Locate the cells, classifying each as a parasitized red blood cell, an uninfected red blood cell, or a white blood cell.
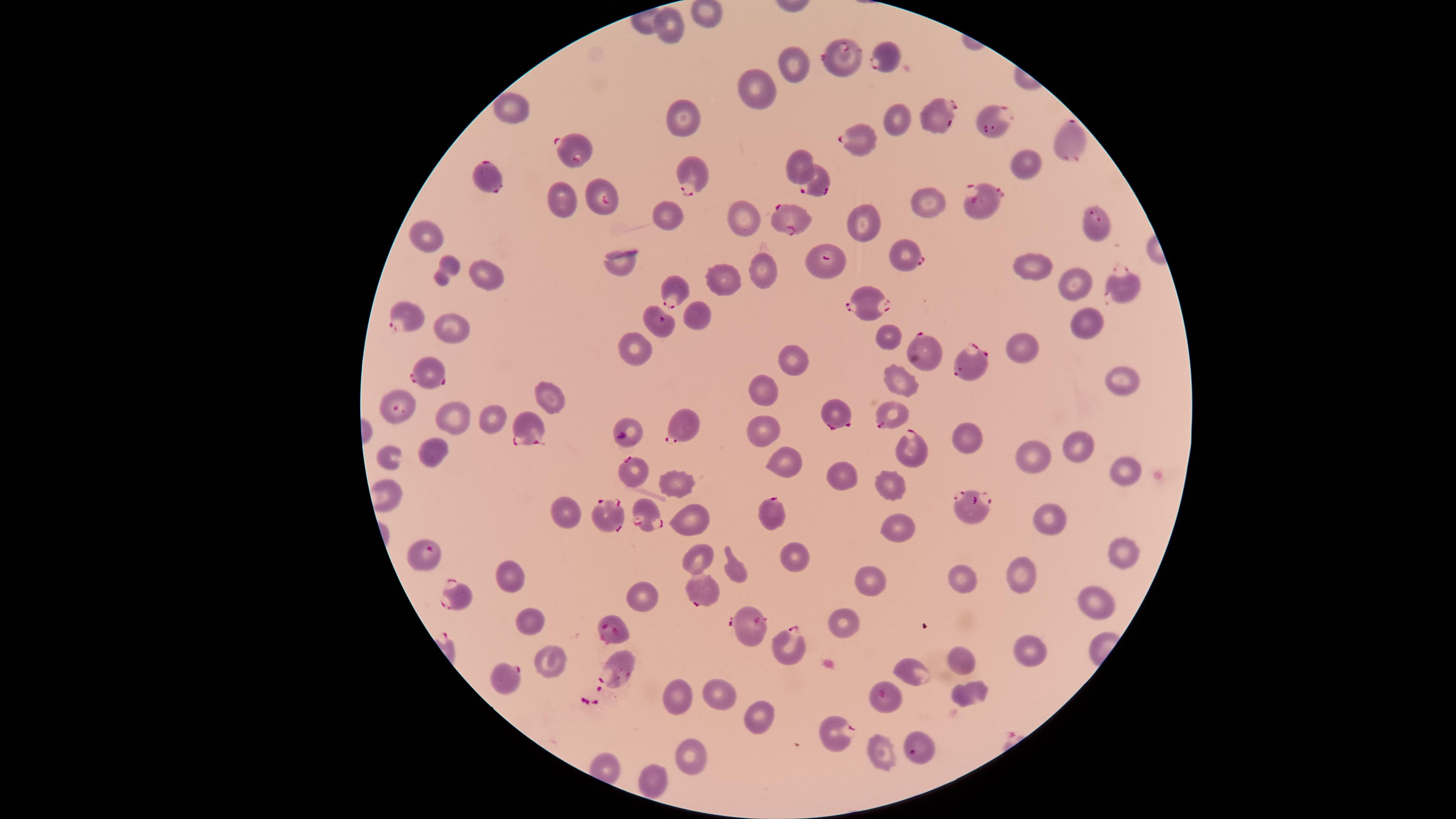

Approximate marker points as {x, y} in pixels.
Parasitized red blood cells: {844, 57}, {882, 57}, {935, 114}, {997, 121}, {1064, 140}, {859, 141}, {577, 145}, {692, 174}, {486, 177}, {816, 181}, {606, 195}, {984, 203}, {786, 221}, {1099, 229}, {898, 249}, {825, 265}, {1121, 286}, {678, 289}, {867, 305}, {407, 319}, {661, 323}, {924, 354}, {971, 361}, {428, 369}, {396, 411}, {836, 414}, {893, 414}, {528, 424}, {688, 425}, {635, 431}, {911, 447}, {630, 467}, {973, 502}, {643, 511}, {769, 513}, {617, 518}, {424, 557}, {455, 590}, {697, 591}, {612, 629}, {748, 631}, {791, 644}, {617, 671}, {501, 684}, {889, 700}, {837, 725}, {914, 753}.
Uninfected red blood cells: {701, 12}, {669, 26}, {790, 58}, {758, 85}, {511, 107}, {683, 114}, {894, 118}, {1024, 163}, {797, 165}, {560, 198}, {928, 201}, {663, 212}, {743, 217}, {864, 222}, {426, 237}, {621, 260}, {761, 267}, {1032, 268}, {441, 271}, {484, 273}, {727, 278}, {1071, 281}, {699, 315}, {1086, 316}, {450, 329}, {884, 333}, {634, 347}, {1027, 347}, {789, 357}, {901, 375}, {1116, 381}, {767, 387}, {543, 396}, {494, 416}, {449, 417}, {764, 435}, {969, 440}, {1074, 446}, {427, 448}, {389, 456}, {1031, 457}, {788, 459}, {1124, 465}, {846, 473}, {676, 481}, {887, 484}, {562, 510}, {691, 517}, {1049, 520}, {898, 526}, {1120, 552}, {698, 557}, {790, 558}, {509, 571}, {737, 571}, {1020, 573}, {961, 576}, {870, 580}, {640, 593}, {1093, 599}, {524, 617}, {843, 622}, {1025, 645}, {545, 655}, {959, 656}, {916, 671}, {716, 687}, {970, 691}, {680, 696}, {758, 713}, {879, 752}, {690, 754}, {651, 776}.
No white blood cells identified.

Summary:
  - Field of view: single
  - Preparation: thin blood film
  - Species: Plasmodium falciparum
  - Image size: 1456×819 pixels
  - Visible region: circular
  - Capture: smartphone photograph through the microscope eyepiece
  - Stain: Giemsa